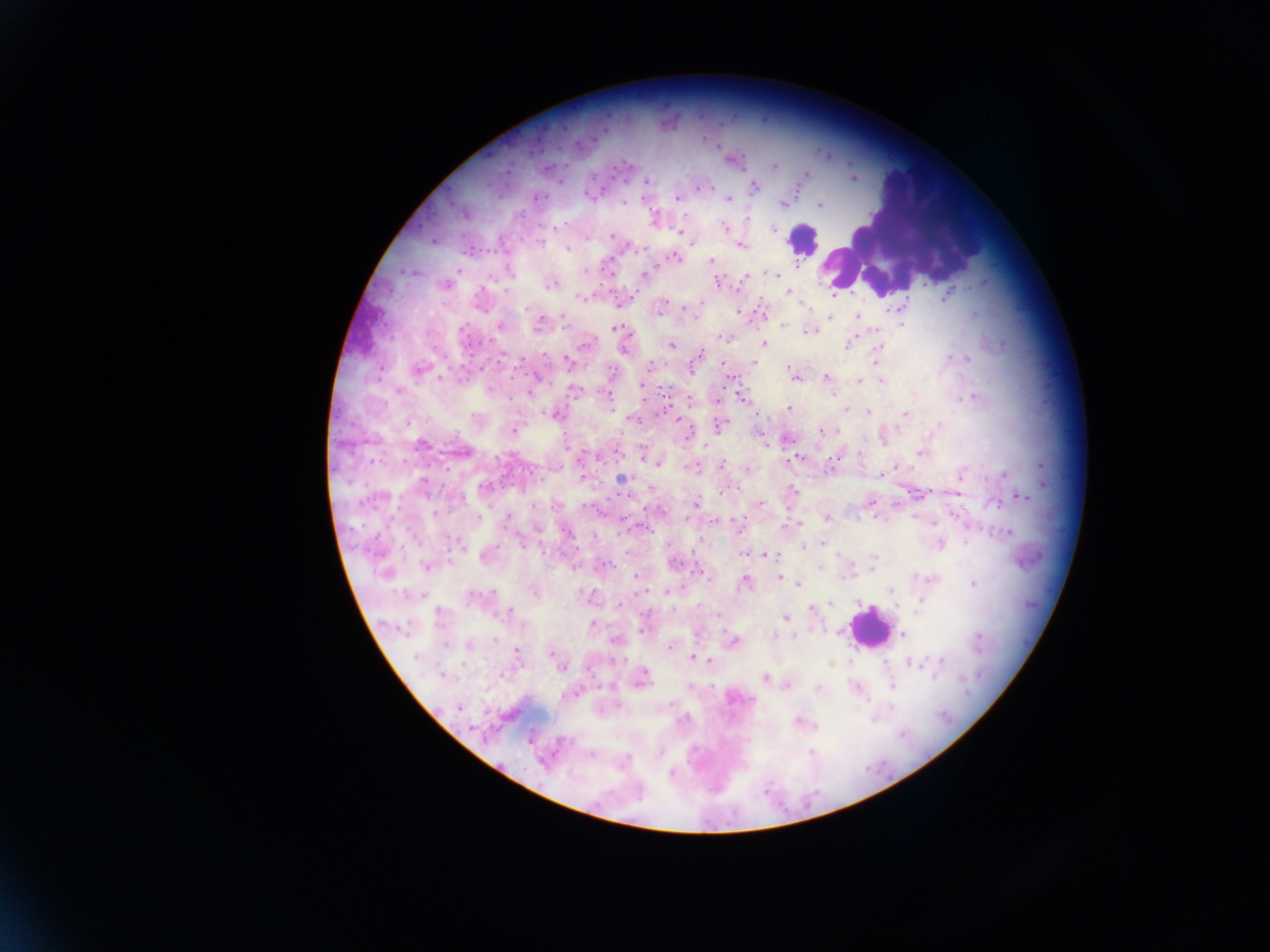
Approximate centers as [x, y] in pixels.
Summary:
  - Leukocyte locations: [804, 240], [869, 628]
  - Malaria parasite locations: [735, 160], [775, 166], [806, 174], [592, 176], [853, 178], [647, 181], [754, 187], [698, 188], [705, 188], [588, 195], [538, 197], [677, 198], [728, 199], [622, 203], [782, 205], [820, 205], [521, 215], [654, 218], [748, 219], [556, 227], [724, 227], [774, 230], [680, 232], [612, 235], [433, 241], [541, 244], [741, 246], [567, 248], [646, 250], [675, 257], [711, 260], [797, 266], [458, 271], [584, 271], [647, 271], [413, 272], [509, 272], [645, 274], [773, 274], [745, 278], [716, 283], [551, 284], [445, 286], [976, 286], [506, 292], [788, 292], [832, 296], [945, 297], [581, 298], [662, 303], [700, 304], [802, 305], [903, 306], [888, 310], [738, 312], [975, 314], [857, 315], [562, 317], [829, 317], [540, 324], [902, 324], [499, 325], [565, 325], [783, 326], [615, 327], [462, 329], [807, 332], [724, 338], [585, 344], [764, 344], [671, 345], [847, 345], [624, 348], [877, 348], [700, 353], [544, 356], [949, 358], [956, 358], [967, 358], [522, 359], [567, 361], [876, 361], [754, 362], [722, 364], [649, 366], [788, 368], [418, 371], [441, 378], [535, 378], [826, 378], [796, 379], [860, 381], [882, 381], [643, 384], [490, 389], [573, 391], [400, 392], [608, 396], [740, 397], [974, 397], [511, 398], [717, 400], [788, 408], [846, 410], [868, 412], [905, 414], [555, 415], [632, 420], [680, 422], [719, 425], [939, 425], [514, 430], [821, 431], [686, 434], [786, 438], [422, 444], [764, 445], [704, 446], [921, 453], [643, 456], [797, 458], [651, 461], [657, 463], [722, 465], [895, 466], [689, 467], [747, 470], [1004, 474], [881, 475], [960, 477], [621, 479], [423, 484], [484, 486], [793, 491], [724, 492], [1022, 498], [871, 503], [696, 504], [760, 504], [994, 504], [478, 517], [508, 517], [827, 517], [686, 519], [716, 522], [799, 523], [933, 524], [644, 527], [566, 532], [1008, 533], [966, 541], [522, 542], [822, 544], [940, 545], [804, 547], [626, 553], [743, 555], [769, 555], [485, 557], [872, 559], [674, 563], [605, 564], [426, 567], [819, 569], [699, 571], [384, 574], [635, 577], [779, 577], [933, 579], [745, 582], [795, 582], [798, 584], [973, 584], [891, 590], [491, 592], [534, 592], [667, 592], [472, 597], [920, 601], [830, 603], [619, 605], [895, 607], [672, 609], [811, 610], [917, 611], [511, 612], [439, 613], [720, 616], [785, 619], [592, 625], [522, 626], [644, 630], [903, 634], [773, 636], [794, 636], [979, 638], [496, 640], [615, 641], [734, 641], [445, 644], [469, 645], [669, 648], [516, 651], [552, 655], [693, 657], [415, 658], [942, 660], [710, 661], [911, 664], [561, 667], [442, 675], [644, 675], [934, 677], [764, 678], [788, 685], [893, 685], [819, 688], [459, 707], [892, 708], [683, 720], [798, 721], [660, 752], [811, 752], [591, 755], [628, 759], [671, 774]
  - Field of view: single
  - Image size: 1270×952 pixels
  - Country: Ghana
  - Preparation: thick blood smear
  - Capture: mobile-phone photograph through a microscope